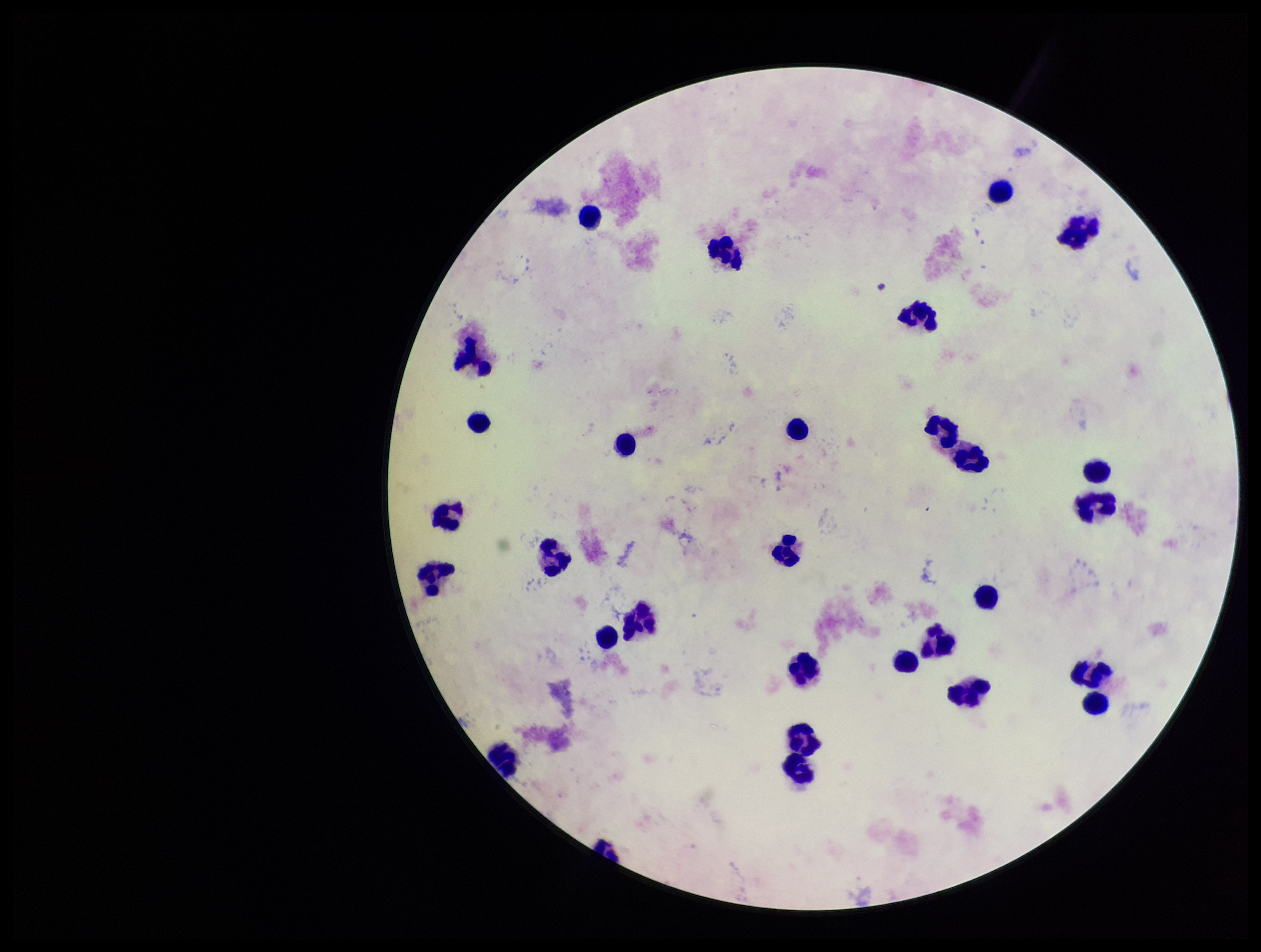

Summary:
  - Parasite count: 0
  - Patient malaria status: negative
  - Plasmodium parasites: none seen
  - Capture: smartphone photograph through the microscope eyepiece
  - Preparation: thick
  - Leukocyte count: 30
  - Field of view: single
  - Stain: Giemsa
  - Image size: 1261×952 pixels